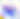 Photomicrograph. Toxoplasma gondii is seen. Captured at 400x magnification.